Classify this cell by malaria status.
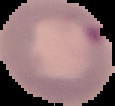

It is parasitized.

Summary:
  - Preparation: thin blood film
  - Image type: cell region segmented out of the field of view; surrounding area masked to black
  - Image size: 115×106 pixels